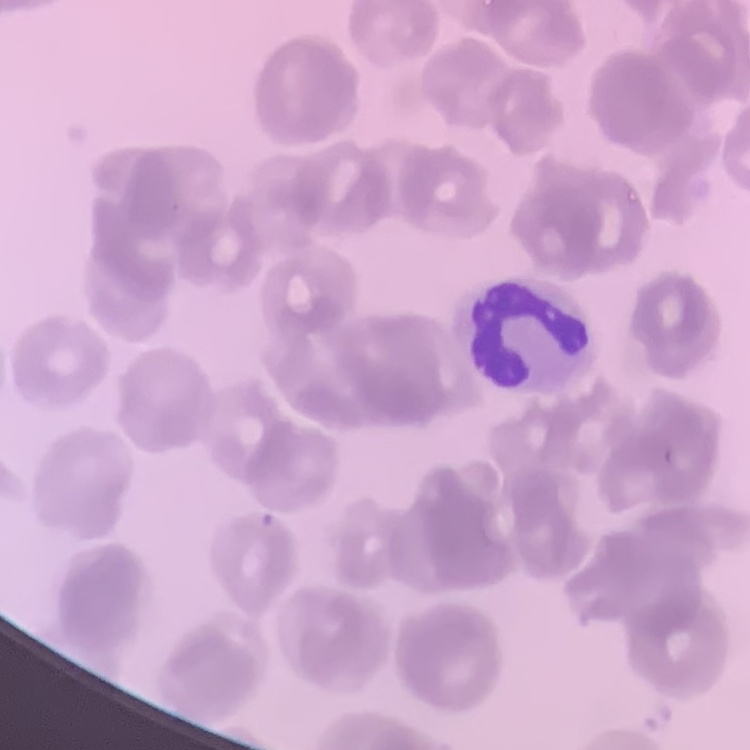 The erythrocytes exhibit rouleaux formation. Square crop of a larger photomicrograph. Stained with either Field's or Giemsa. Thin blood film.